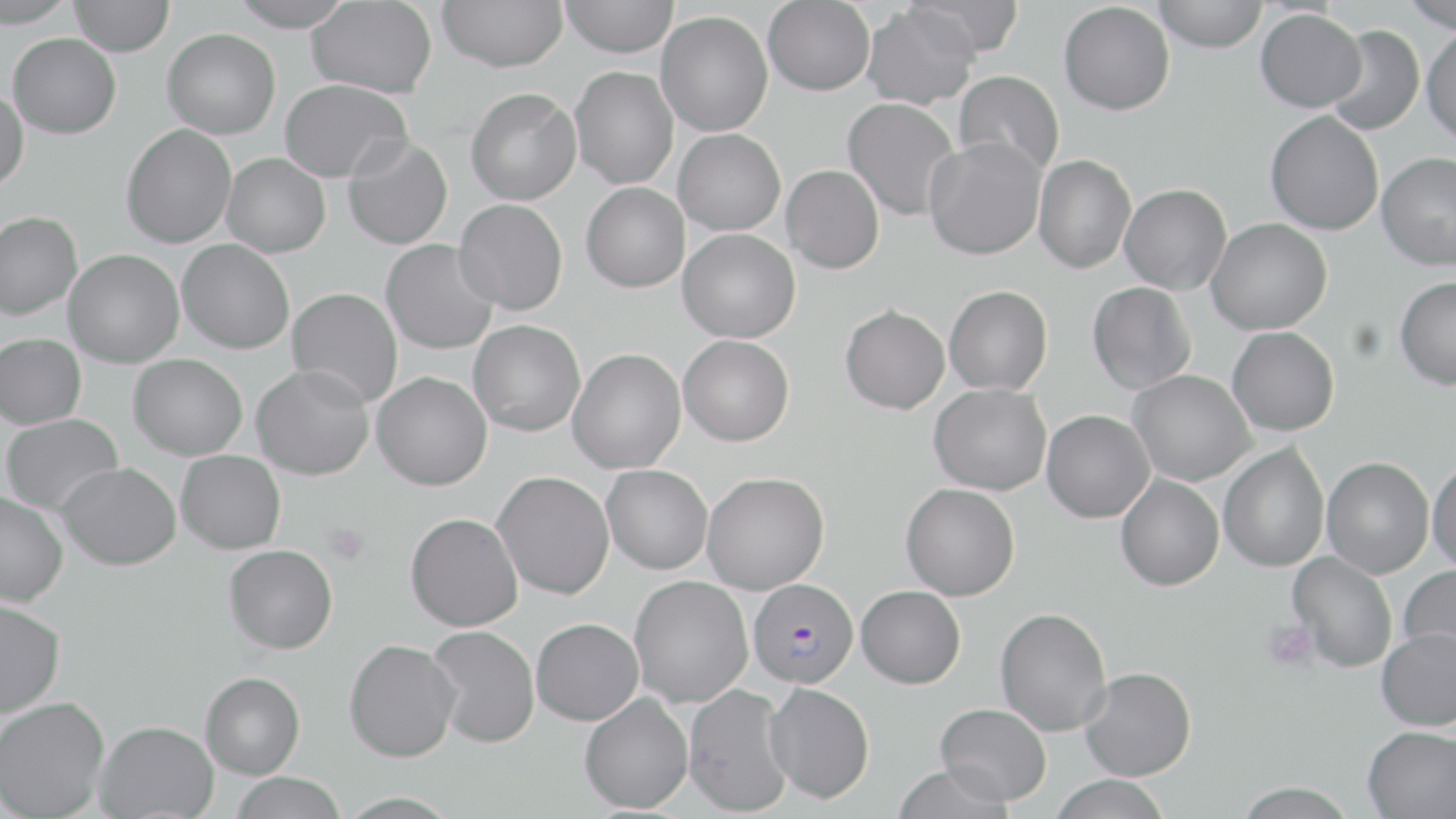

Summary:
  - Coordinate format: approximate bounding boxes as (x1,y1)-(x2,y2) corner pairs in pixels
  - Uninfected red blood cell locations: (0,0)-(77,28), (70,0)-(174,56), (227,0)-(355,31), (307,0)-(437,98), (438,0)-(567,72), (560,0)-(678,57), (763,0)-(875,95), (906,0)-(1024,59), (1152,0)-(1268,52), (1401,0)-(1456,32), (1059,2)-(1175,115), (862,4)-(979,109), (1255,9)-(1366,112), (656,11)-(773,136), (1325,24)-(1424,135), (1422,26)-(1456,146), (162,28)-(281,138), (8,33)-(121,138), (570,67)-(678,189), (953,70)-(1064,178), (280,78)-(412,182), (0,87)-(28,191), (465,87)-(581,205), (842,97)-(961,220), (1265,111)-(1384,235), (121,123)-(237,248), (673,128)-(786,235), (342,136)-(453,249), (923,137)-(1046,260), (1376,152)-(1456,271), (222,153)-(331,258), (1033,154)-(1136,273), (781,165)-(884,274), (581,181)-(690,292), (1120,183)-(1232,295), (453,199)-(567,315), (0,210)-(82,320), (1207,217)-(1332,334), (678,228)-(801,343), (177,239)-(294,353), (381,239)-(499,354), (64,249)-(184,367), (1395,276)-(1456,389), (1087,282)-(1196,394), (944,285)-(1052,395), (286,287)-(403,407), (840,305)-(949,414), (468,320)-(585,436), (1227,326)-(1339,436), (0,333)-(86,428), (678,334)-(794,446), (568,348)-(686,473), (129,354)-(248,460), (250,364)-(375,480), (1128,369)-(1256,486), (372,371)-(492,490), (928,383)-(1051,495), (1042,409)-(1155,523), (1,414)-(123,515), (1218,443)-(1329,572), (176,450)-(285,553), (1322,457)-(1434,578), (1427,457)-(1456,575), (56,462)-(180,570), (602,464)-(713,574), (492,470)-(614,599), (702,471)-(829,594), (1116,474)-(1224,590), (901,483)-(1020,600), (0,493)-(68,606), (405,512)-(523,631), (224,544)-(338,653), (1288,552)-(1397,672), (1399,564)-(1456,668), (630,575)-(753,707), (856,585)-(965,688), (0,599)-(65,717), (994,607)-(1112,736), (531,618)-(643,725), (427,625)-(540,748), (1376,627)-(1456,731), (344,639)-(462,762), (1079,666)-(1196,780), (201,671)-(306,778), (765,682)-(875,803), (683,684)-(794,815), (579,692)-(693,813), (0,697)-(109,819), (934,703)-(1052,805), (95,720)-(219,818), (1363,726)-(1456,819), (890,763)-(1017,819), (230,772)-(347,819), (1048,774)-(1173,818), (1233,782)-(1358,819)
  - Platelet locations: (322,522)-(370,566), (1263,619)-(1318,672)
  - Plasmodium falciparum-infected red blood cell locations: (748,578)-(858,688)
  - Slide-level diagnosis: Plasmodium falciparum
  - Stain: May-Grünwald-Giemsa
  - Modality: light microscopy
  - Image size: 1456×819 pixels
  - Preparation: thin blood smear
  - Magnification: 1000x
  - Field of view: one of a larger specimen